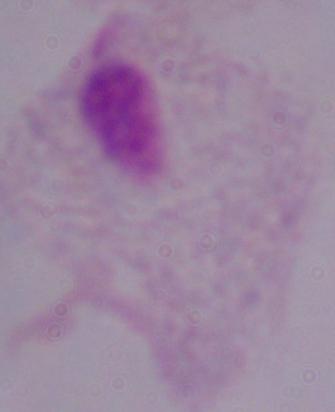

A trichomonad is seen. Photomicrograph. Captured at 1000x magnification.